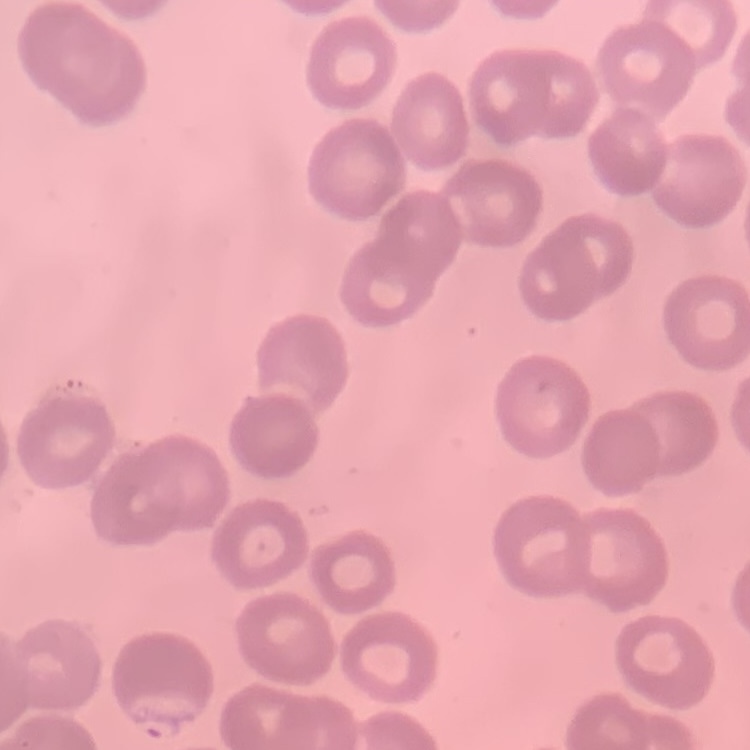

Summary:
  - Red blood cell morphology: no rouleaux formation
  - Image type: one tile cut from a larger photomicrograph
  - Stain: Field's or Giemsa
  - Preparation: thin peripheral smear